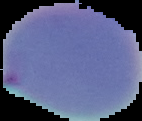
image type = segmented cell region on a black background
preparation = thin blood film
result = Plasmodium parasites detected
image size = 142×121 pixels